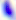
Summary:
  - Modality: photomicrograph
  - Identification: Toxoplasma gondii
  - Magnification: 400x